Report the malaria status of this cell.
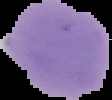
It is uninfected.

{
  "image_size": "112×100 pixels",
  "preparation": "thin blood smear",
  "image_type": "segmented cell region on a black background"
}